Classify this cell by malaria status.
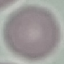
Uninfected.

{
  "image_type": "cell patch, automatically extracted from a larger field of view and resized to 64 × 64 pixels",
  "preparation": "thin smear",
  "capture": "smartphone camera at the microscope eyepiece",
  "stain": "Giemsa"
}